Outline each Plasmodium vivax-infected red blood cell.
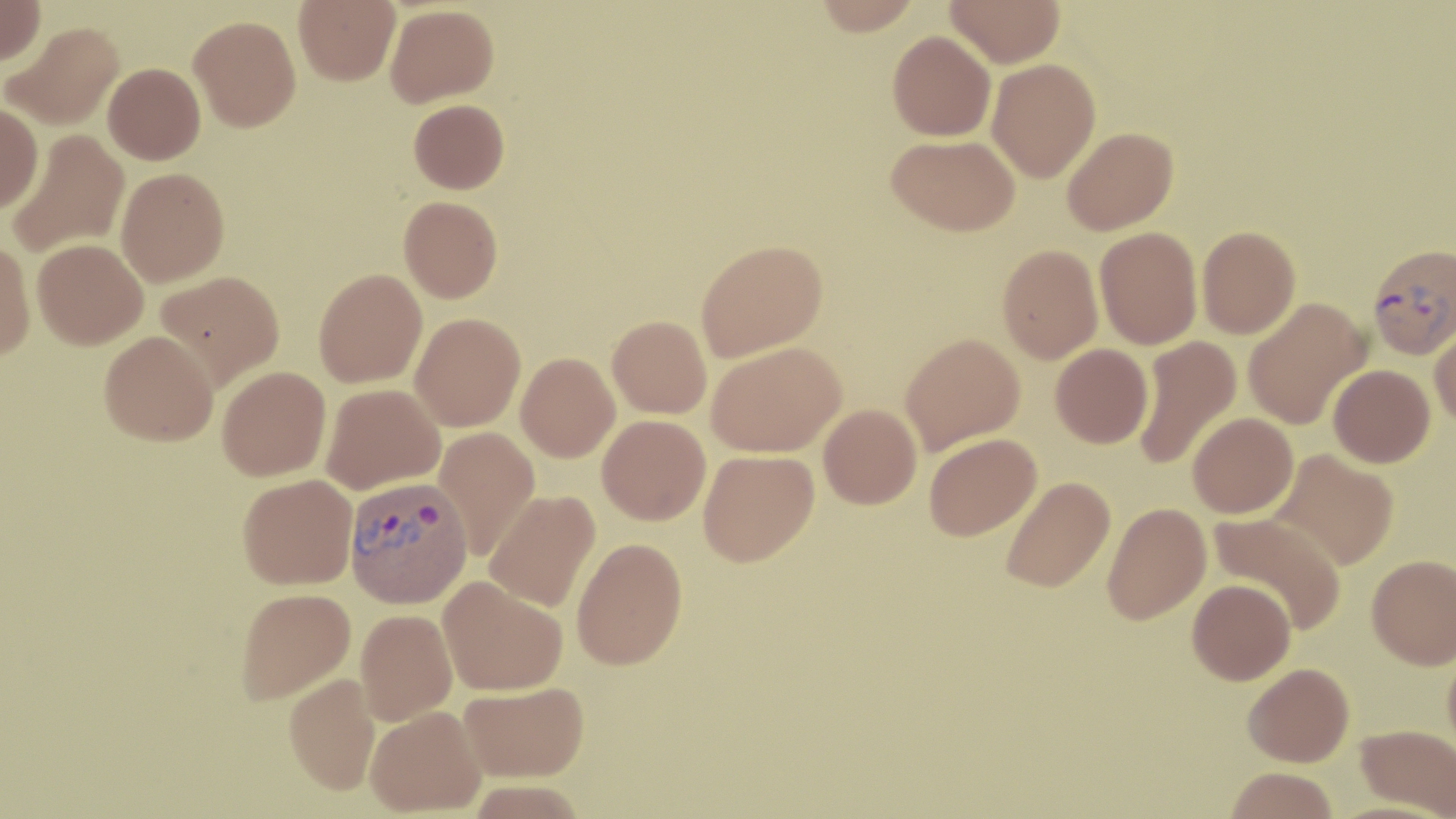
Approximate bounding boxes as named x1/y1/x2/y2 corners in pixels.
Plasmodium vivax-infected red blood cells: (x1=1367, y1=243, x2=1455, y2=359), (x1=343, y1=475, x2=472, y2=608).

{
  "slide_level_diagnosis": "Plasmodium vivax",
  "image_size": "1456×819 pixels",
  "preparation": "thin blood film",
  "modality": "optical microscopy",
  "magnification": "1000x",
  "stain": "May-Grünwald-Giemsa",
  "field_of_view": "one of a larger specimen",
  "uninfected_red_blood_cell_locations": "approximate bounding boxes as named x1/y1/x2/y2 corners in pixels: (x1=0, y1=0, x2=45, y2=66), (x1=294, y1=0, x2=399, y2=85), (x1=813, y1=0, x2=923, y2=35), (x1=945, y1=0, x2=1065, y2=67), (x1=385, y1=4, x2=498, y2=107), (x1=189, y1=16, x2=301, y2=131), (x1=2, y1=21, x2=125, y2=131), (x1=887, y1=31, x2=995, y2=141), (x1=987, y1=59, x2=1101, y2=183), (x1=104, y1=62, x2=205, y2=164), (x1=409, y1=99, x2=509, y2=193), (x1=0, y1=102, x2=43, y2=212), (x1=1062, y1=126, x2=1178, y2=235), (x1=7, y1=129, x2=129, y2=258), (x1=886, y1=134, x2=1019, y2=235), (x1=116, y1=167, x2=229, y2=287), (x1=399, y1=196, x2=502, y2=302), (x1=1197, y1=226, x2=1300, y2=339), (x1=1095, y1=227, x2=1202, y2=349), (x1=32, y1=238, x2=148, y2=349), (x1=695, y1=239, x2=827, y2=362), (x1=0, y1=241, x2=36, y2=360), (x1=997, y1=244, x2=1104, y2=363), (x1=313, y1=269, x2=427, y2=388), (x1=155, y1=270, x2=284, y2=390), (x1=1241, y1=297, x2=1373, y2=431), (x1=410, y1=313, x2=525, y2=431), (x1=608, y1=315, x2=712, y2=418), (x1=1430, y1=320, x2=1456, y2=428), (x1=99, y1=331, x2=218, y2=445), (x1=900, y1=333, x2=1025, y2=455), (x1=1133, y1=336, x2=1242, y2=470), (x1=707, y1=342, x2=845, y2=457), (x1=1050, y1=344, x2=1153, y2=447), (x1=516, y1=352, x2=620, y2=462), (x1=1328, y1=364, x2=1435, y2=468), (x1=217, y1=366, x2=331, y2=480), (x1=322, y1=383, x2=445, y2=494), (x1=818, y1=404, x2=922, y2=508), (x1=1187, y1=412, x2=1299, y2=519), (x1=597, y1=414, x2=711, y2=524), (x1=433, y1=426, x2=540, y2=558), (x1=924, y1=433, x2=1041, y2=540), (x1=1270, y1=448, x2=1399, y2=570), (x1=698, y1=449, x2=819, y2=566), (x1=238, y1=474, x2=357, y2=589), (x1=1000, y1=475, x2=1115, y2=593), (x1=484, y1=489, x2=601, y2=612), (x1=1102, y1=503, x2=1212, y2=625), (x1=1209, y1=510, x2=1347, y2=634), (x1=571, y1=537, x2=687, y2=669), (x1=1367, y1=554, x2=1456, y2=669), (x1=438, y1=576, x2=567, y2=696), (x1=1187, y1=578, x2=1296, y2=685), (x1=236, y1=587, x2=355, y2=704), (x1=355, y1=609, x2=457, y2=725), (x1=1443, y1=643, x2=1456, y2=766), (x1=1243, y1=663, x2=1355, y2=766), (x1=284, y1=672, x2=381, y2=794), (x1=459, y1=680, x2=588, y2=781), (x1=366, y1=706, x2=486, y2=816), (x1=1355, y1=723, x2=1456, y2=817), (x1=1225, y1=766, x2=1338, y2=819)"
}